Name the blood parasite species.
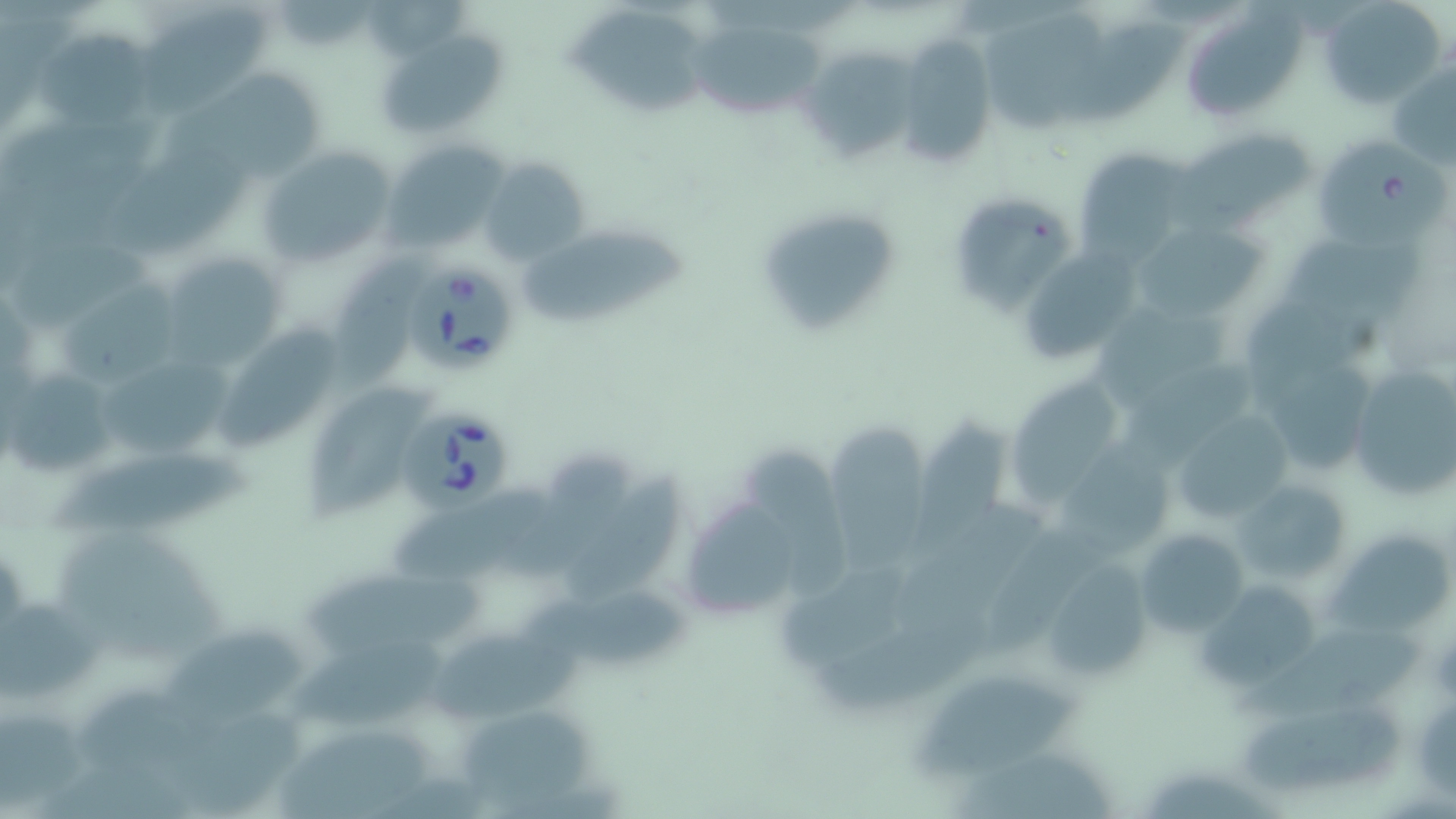

Babesia divergens.

Approximate bounding boxes as named x1/y1/x2/y2 corners in pixels. Uninfected red blood cell locations: (x1=1320, y1=0, x2=1444, y2=108), (x1=365, y1=1, x2=476, y2=58), (x1=566, y1=7, x2=709, y2=115), (x1=977, y1=7, x2=1109, y2=130), (x1=130, y1=11, x2=277, y2=117), (x1=1188, y1=11, x2=1310, y2=119), (x1=678, y1=17, x2=830, y2=113), (x1=1062, y1=21, x2=1195, y2=125), (x1=33, y1=28, x2=159, y2=130), (x1=894, y1=32, x2=995, y2=168), (x1=379, y1=33, x2=507, y2=134), (x1=800, y1=47, x2=914, y2=166), (x1=161, y1=63, x2=330, y2=178), (x1=1389, y1=64, x2=1456, y2=167), (x1=1181, y1=130, x2=1315, y2=227), (x1=1317, y1=135, x2=1449, y2=248), (x1=386, y1=140, x2=511, y2=255), (x1=96, y1=146, x2=259, y2=265), (x1=257, y1=146, x2=397, y2=266), (x1=1072, y1=147, x2=1194, y2=261), (x1=479, y1=158, x2=588, y2=265), (x1=944, y1=193, x2=1071, y2=313), (x1=756, y1=204, x2=902, y2=341), (x1=1129, y1=221, x2=1263, y2=324), (x1=1282, y1=226, x2=1434, y2=332), (x1=519, y1=228, x2=702, y2=324), (x1=3, y1=237, x2=162, y2=326), (x1=1019, y1=237, x2=1157, y2=358), (x1=157, y1=253, x2=288, y2=366), (x1=323, y1=259, x2=424, y2=409), (x1=60, y1=269, x2=196, y2=383), (x1=1090, y1=299, x2=1243, y2=406), (x1=217, y1=323, x2=339, y2=454), (x1=96, y1=347, x2=243, y2=456), (x1=1271, y1=355, x2=1380, y2=473), (x1=1347, y1=357, x2=1456, y2=505), (x1=1127, y1=365, x2=1260, y2=469), (x1=3, y1=369, x2=116, y2=477), (x1=1014, y1=379, x2=1115, y2=508), (x1=303, y1=386, x2=429, y2=528), (x1=1167, y1=409, x2=1291, y2=530), (x1=910, y1=414, x2=1011, y2=555), (x1=826, y1=421, x2=924, y2=572), (x1=1068, y1=432, x2=1185, y2=556), (x1=42, y1=444, x2=267, y2=536), (x1=737, y1=445, x2=846, y2=594), (x1=508, y1=446, x2=650, y2=582), (x1=566, y1=467, x2=684, y2=606), (x1=1229, y1=471, x2=1359, y2=593), (x1=387, y1=478, x2=550, y2=582), (x1=896, y1=501, x2=1054, y2=639), (x1=685, y1=505, x2=798, y2=619), (x1=54, y1=525, x2=231, y2=658), (x1=1134, y1=525, x2=1248, y2=638), (x1=1322, y1=538, x2=1456, y2=627), (x1=782, y1=544, x2=930, y2=666), (x1=303, y1=558, x2=503, y2=650), (x1=1037, y1=560, x2=1156, y2=681), (x1=1199, y1=576, x2=1321, y2=685), (x1=525, y1=583, x2=690, y2=664), (x1=0, y1=597, x2=107, y2=696), (x1=810, y1=613, x2=997, y2=717), (x1=168, y1=621, x2=314, y2=719), (x1=1227, y1=626, x2=1432, y2=719), (x1=295, y1=631, x2=465, y2=728), (x1=434, y1=631, x2=590, y2=727), (x1=918, y1=676, x2=1089, y2=779), (x1=465, y1=701, x2=595, y2=803), (x1=0, y1=705, x2=86, y2=818), (x1=1243, y1=705, x2=1406, y2=791), (x1=279, y1=724, x2=433, y2=819), (x1=960, y1=752, x2=1122, y2=819), (x1=35, y1=756, x2=200, y2=819). Babesia divergens-infected red blood cell locations: (x1=405, y1=263, x2=515, y2=373), (x1=394, y1=406, x2=513, y2=520). Thin blood smear. Image is 1456×819 pixels. 1000x magnification. Light microscopy. May-Grünwald-Giemsa stain. One field of a larger specimen.